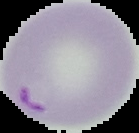

result = Plasmodium parasites identified
image type = cell region segmented out of the field of view; surrounding area masked to black
preparation = thin blood film
image size = 139×133 pixels